Assess this cell for malaria.
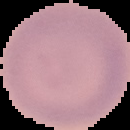
It is uninfected.

Summary:
  - Image type: segmented cell region on a black background
  - Image size: 130×130 pixels
  - Preparation: thin blood smear